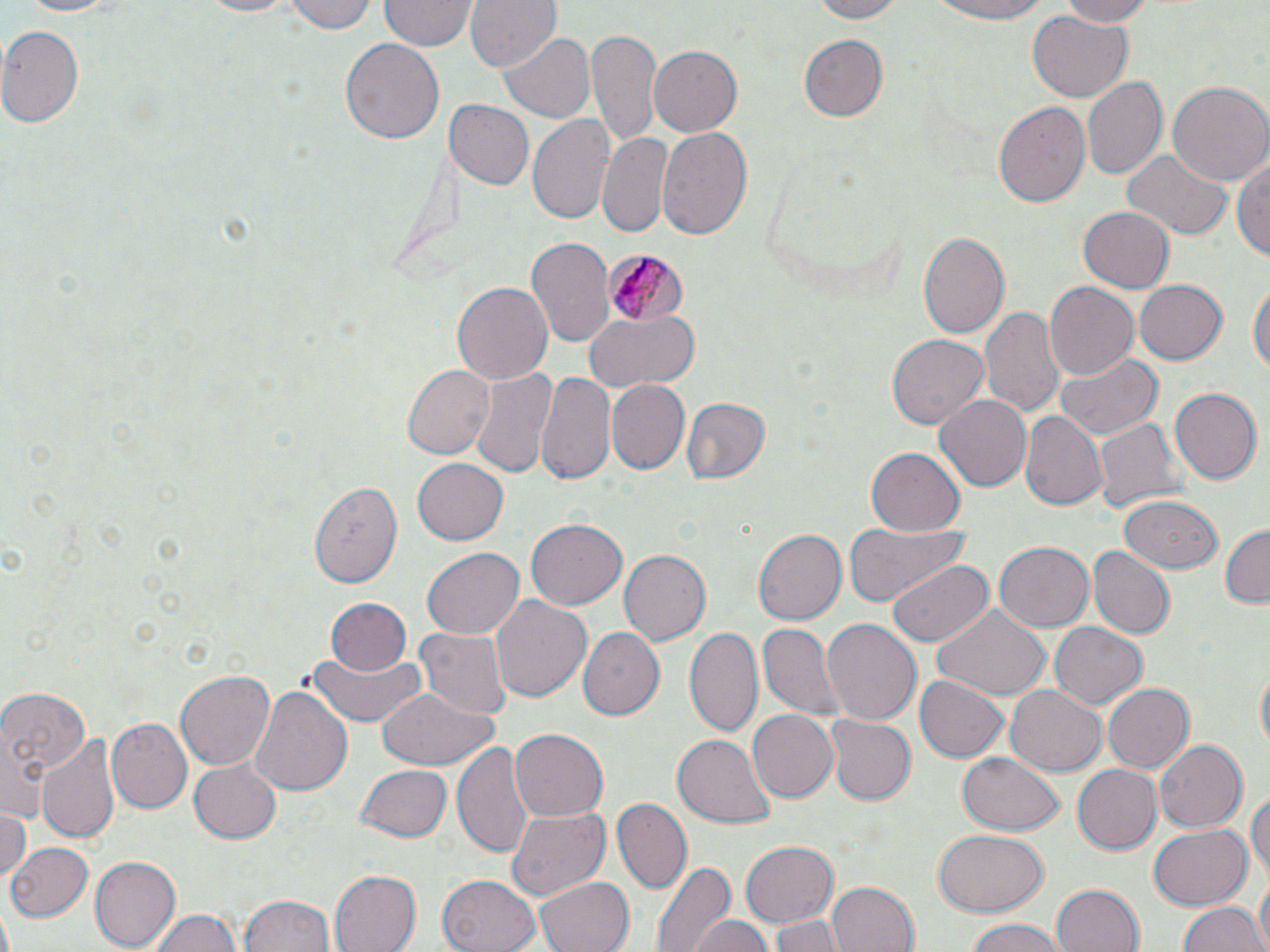

Summary:
  - Coordinate format: approximate bounding boxes as [x1, y1, x2, y2] in pixels
  - Plasmodium malariae-infected red blood cell locations: [606, 248, 686, 327]
  - Uninfected red blood cell locations: [12, 0, 128, 17], [286, 0, 379, 34], [380, 0, 473, 52], [467, 0, 561, 75], [803, 0, 905, 23], [923, 0, 1059, 24], [1053, 0, 1158, 26], [189, 1, 304, 18], [1025, 10, 1132, 102], [0, 24, 83, 130], [587, 29, 662, 148], [795, 33, 892, 121], [500, 34, 594, 122], [342, 38, 442, 147], [646, 45, 741, 137], [1083, 75, 1166, 181], [1167, 79, 1270, 187], [441, 99, 532, 188], [992, 101, 1091, 212], [528, 114, 617, 225], [657, 127, 753, 242], [596, 134, 673, 238], [1122, 148, 1232, 241], [1233, 152, 1270, 268], [1077, 206, 1176, 293], [917, 232, 1008, 339], [526, 237, 614, 348], [1250, 278, 1269, 383], [1135, 279, 1229, 365], [451, 281, 553, 385], [1043, 283, 1138, 379], [980, 304, 1065, 421], [586, 312, 698, 391], [887, 332, 993, 430], [1054, 351, 1162, 443], [401, 363, 496, 460], [469, 365, 559, 483], [537, 372, 614, 483], [605, 379, 688, 474], [1168, 388, 1260, 486], [932, 392, 1032, 494], [679, 398, 770, 485], [1020, 413, 1105, 509], [1091, 417, 1185, 518], [865, 448, 964, 535], [413, 457, 508, 546], [307, 478, 404, 586], [1115, 494, 1221, 573], [526, 518, 628, 609], [841, 521, 969, 605], [1218, 524, 1270, 609], [753, 528, 846, 626], [996, 543, 1094, 631], [420, 547, 525, 639], [617, 548, 710, 645], [1090, 548, 1174, 640], [886, 559, 996, 650], [492, 595, 592, 701], [327, 598, 410, 676], [935, 606, 1050, 697], [821, 616, 923, 726], [1050, 622, 1149, 710], [758, 623, 844, 721], [685, 626, 764, 737], [416, 627, 511, 719], [581, 629, 665, 720], [306, 648, 426, 728], [1255, 666, 1269, 759], [175, 669, 275, 769], [915, 675, 1010, 763], [1103, 682, 1194, 773], [0, 684, 89, 812], [249, 684, 351, 798], [1005, 684, 1106, 775], [375, 686, 499, 772], [746, 709, 839, 803], [823, 715, 915, 805], [106, 719, 192, 814], [510, 729, 608, 821], [672, 731, 773, 827], [39, 732, 118, 844], [1152, 739, 1246, 832], [452, 741, 531, 861], [956, 753, 1065, 836], [187, 760, 281, 842], [1072, 761, 1162, 851], [357, 763, 451, 841], [1248, 787, 1270, 887], [613, 798, 691, 894], [507, 806, 611, 902], [0, 808, 30, 880], [5, 812, 48, 895], [1147, 825, 1250, 909], [932, 829, 1047, 915], [738, 841, 838, 927], [3, 842, 92, 922], [89, 856, 179, 950], [649, 857, 736, 952], [327, 869, 420, 952], [438, 873, 542, 952], [1253, 875, 1269, 952], [533, 877, 632, 952], [826, 879, 920, 952], [1051, 883, 1145, 952], [241, 893, 335, 952], [1178, 899, 1265, 952], [148, 908, 246, 952], [772, 914, 843, 952], [687, 915, 773, 952], [963, 917, 1071, 952]
  - Slide-level diagnosis: Plasmodium malariae
  - Image size: 1270×952 pixels
  - Stain: May-Grünwald-Giemsa
  - Preparation: thin blood film
  - Modality: light microscopy
  - Field of view: one of a larger specimen
  - Magnification: 1000x